Locate every blood parasite and identify its species.
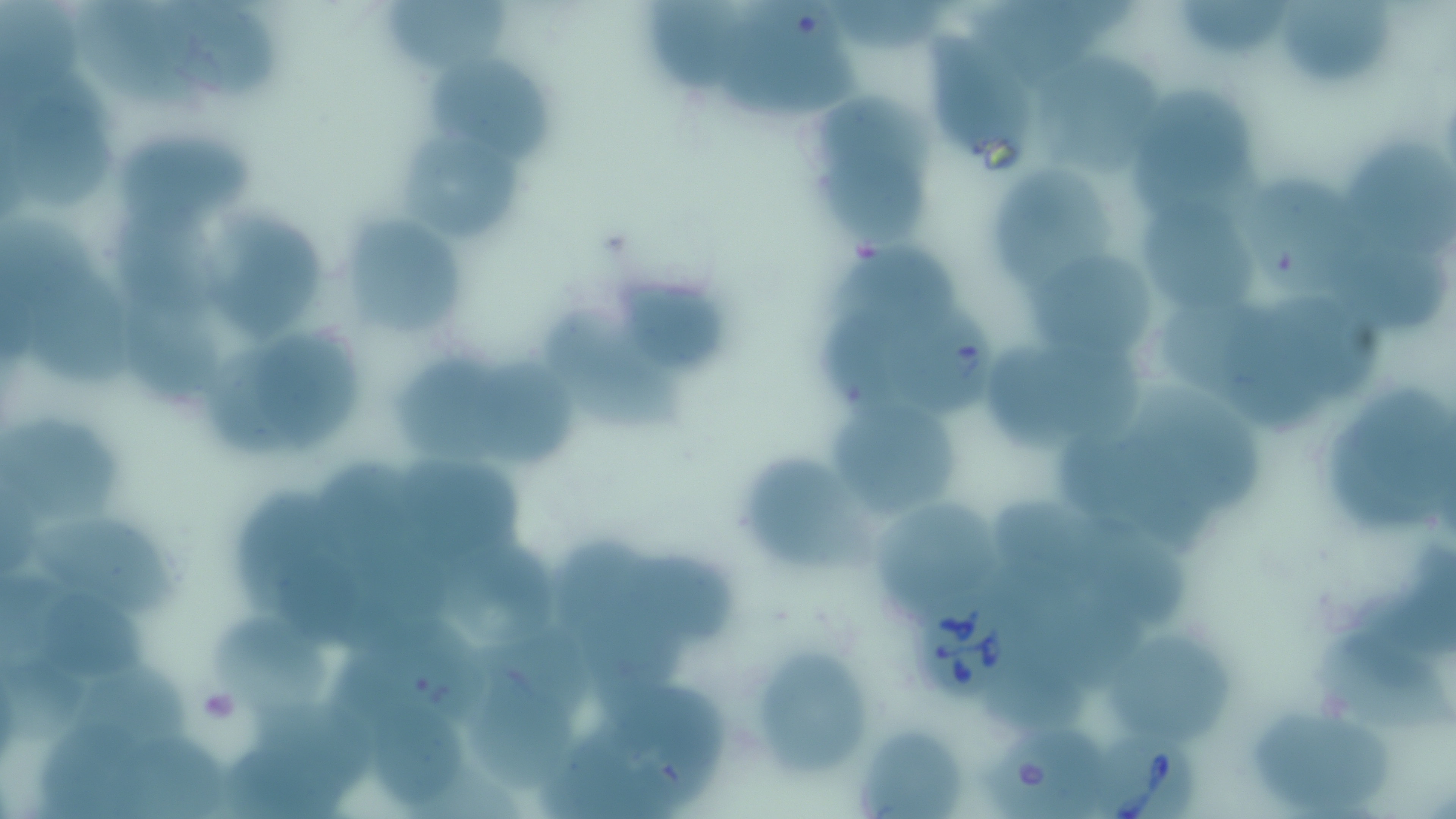
Approximate bounding boxes as (x1,y1)-(x2,y2) corner pairs in pixels.
Babesia divergens-infected red blood cells: (915,598)-(1015,703), (1090,725)-(1200,818).
No Plasmodium falciparum, Plasmodium ovale, Plasmodium malariae, Plasmodium vivax, or Trypanosoma brucei observed.

Summary:
  - Platelet locations: (199,685)-(240,735)
  - Uninfected red blood cell locations: (0,0)-(92,96), (156,0)-(284,101), (831,0)-(956,51), (991,0)-(1135,58), (1280,0)-(1396,83), (74,1)-(199,108), (387,1)-(512,71), (725,1)-(865,122), (1179,2)-(1288,59), (642,3)-(756,93), (931,29)-(1036,159), (1030,43)-(1158,173), (421,49)-(554,171), (1139,78)-(1261,217), (10,84)-(114,210), (824,92)-(945,173), (116,122)-(258,232), (401,133)-(527,249), (1338,136)-(1456,246), (817,152)-(925,250), (993,157)-(1117,291), (1240,166)-(1366,294), (1138,192)-(1253,315), (109,198)-(234,313), (202,199)-(326,342), (344,210)-(464,335), (0,215)-(96,324), (1342,239)-(1450,330), (1031,249)-(1153,363), (831,250)-(966,340), (23,261)-(141,389), (616,271)-(730,378), (1276,292)-(1390,391), (880,300)-(999,418), (536,301)-(686,431), (1155,301)-(1257,397), (133,302)-(236,406), (828,308)-(920,410), (1226,310)-(1328,429), (249,325)-(368,440), (206,338)-(298,458), (396,343)-(514,470), (990,343)-(1166,448), (478,357)-(580,468), (1138,382)-(1273,508), (1329,390)-(1448,534), (838,397)-(956,518), (0,411)-(121,529), (1058,435)-(1215,547), (729,448)-(866,577), (404,453)-(533,558), (324,462)-(425,574), (242,487)-(320,606), (998,493)-(1114,591), (878,495)-(1009,625), (35,511)-(188,615), (1089,527)-(1193,626), (557,534)-(653,642), (439,537)-(565,656), (615,547)-(750,651), (1370,549)-(1453,656), (283,556)-(367,642), (0,576)-(75,663), (42,596)-(153,684), (586,609)-(688,701), (208,610)-(339,721), (347,616)-(498,725), (1103,625)-(1238,744), (1307,627)-(1456,749), (744,643)-(879,776), (5,658)-(88,740), (82,659)-(197,747), (476,660)-(580,797), (985,670)-(1093,733), (609,681)-(730,795), (361,688)-(465,807), (1257,706)-(1403,810), (257,710)-(373,794), (41,716)-(147,819), (544,722)-(674,819), (983,725)-(1120,817), (854,728)-(967,817), (129,734)-(236,819), (227,739)-(339,819)
  - Slide-level diagnosis: Babesia divergens
  - Preparation: thin blood film
  - Modality: light microscopy
  - Magnification: 1000x
  - Image size: 1456×819 pixels
  - Stain: May-Grünwald-Giemsa
  - Field of view: single